Locate and identify every blood parasite.
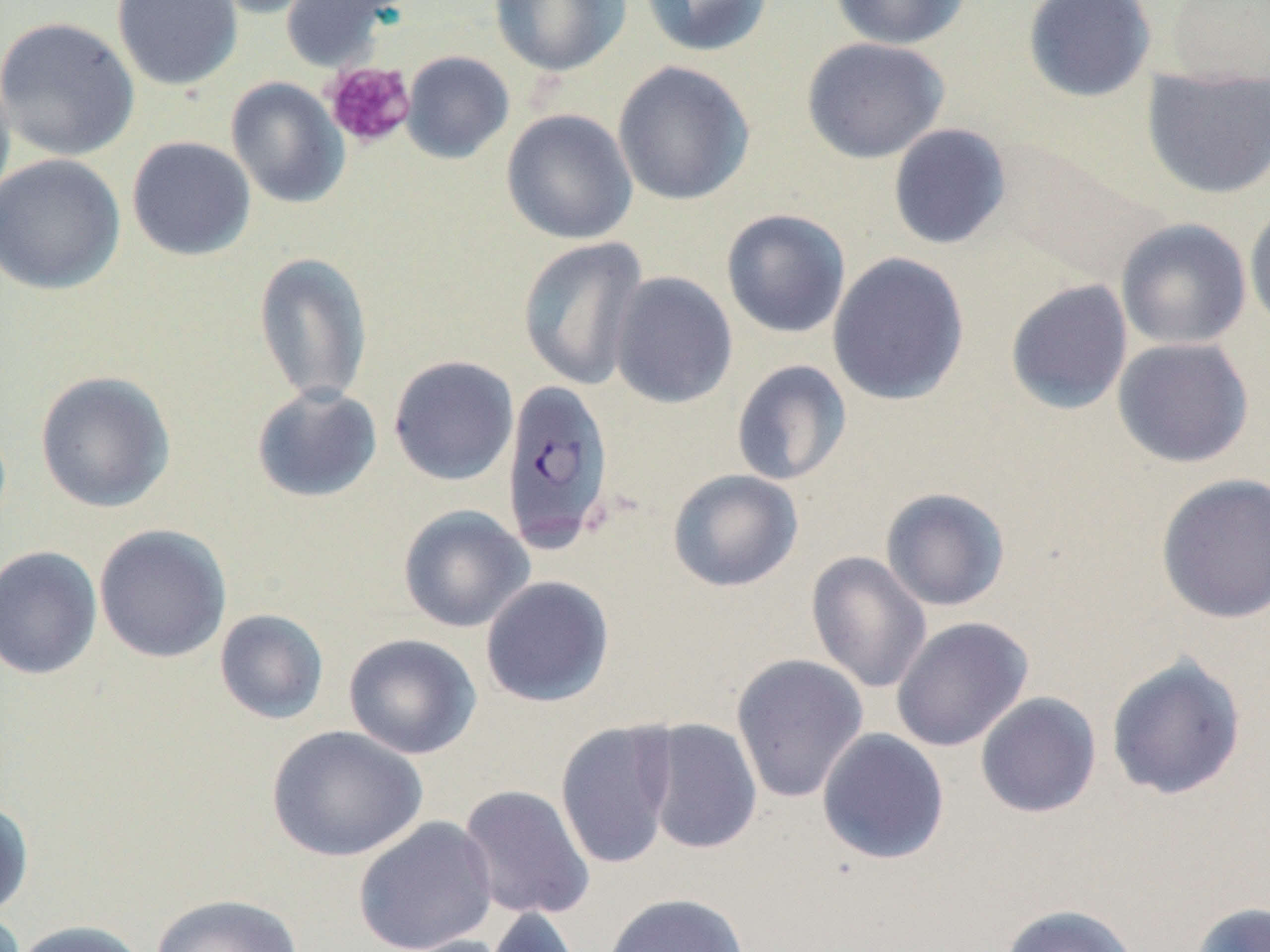
Approximate bounding boxes as (x1,y1)-(x2,y2) corner pairs in pixels.
Plasmodium falciparum-infected red blood cells: (500,378)-(615,552).
No Plasmodium ovale, Plasmodium malariae, Plasmodium vivax, Babesia divergens, or Trypanosoma brucei observed.

Uninfected red blood cell locations: (112,0)-(243,91), (201,0)-(328,19), (279,0)-(404,72), (490,0)-(630,77), (639,0)-(774,58), (828,0)-(972,50), (1022,0)-(1157,104), (1164,0)-(1270,89), (0,16)-(140,161), (802,37)-(950,164), (400,51)-(514,164), (0,60)-(16,214), (612,60)-(754,206), (1140,66)-(1270,200), (226,77)-(349,209), (501,109)-(638,245), (887,123)-(1012,250), (127,135)-(256,261), (0,154)-(125,295), (1244,202)-(1270,335), (721,208)-(851,339), (1115,218)-(1251,350), (517,237)-(649,391), (253,251)-(373,406), (827,252)-(970,406), (609,271)-(737,409), (1004,279)-(1133,415), (1112,337)-(1254,468), (388,355)-(519,486), (731,359)-(852,486), (34,370)-(176,513), (251,384)-(382,504), (667,469)-(803,592), (1155,473)-(1270,624), (879,487)-(1011,612), (398,504)-(535,633), (93,524)-(232,663), (0,545)-(103,680), (806,551)-(932,694), (479,575)-(615,708), (214,608)-(329,725), (890,615)-(1033,752), (343,632)-(482,760), (730,653)-(869,803), (1105,654)-(1247,801), (975,692)-(1102,818), (641,717)-(763,855), (555,719)-(678,870), (266,725)-(427,862), (817,728)-(950,865), (458,783)-(595,921), (0,797)-(34,918), (352,816)-(499,952), (601,891)-(750,952), (150,893)-(304,952), (1189,901)-(1270,952), (998,904)-(1141,952), (482,905)-(584,952), (11,920)-(150,952), (386,934)-(516,952). Platelet locations: (322,61)-(416,149). Slide-level diagnosis: Plasmodium falciparum. Single field of view. Thin blood smear. May-Grünwald-Giemsa-stained preparation. Light microscopy. 1000x magnification. Image is 1270×952 pixels.